Classify this cell by malaria status.
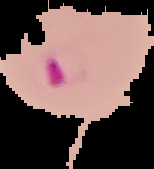
Parasitized.

Summary:
  - Preparation: thin blood film
  - Image type: cell region segmented out of the field of view; surrounding area masked to black
  - Image size: 154×169 pixels